State the blood parasite species.
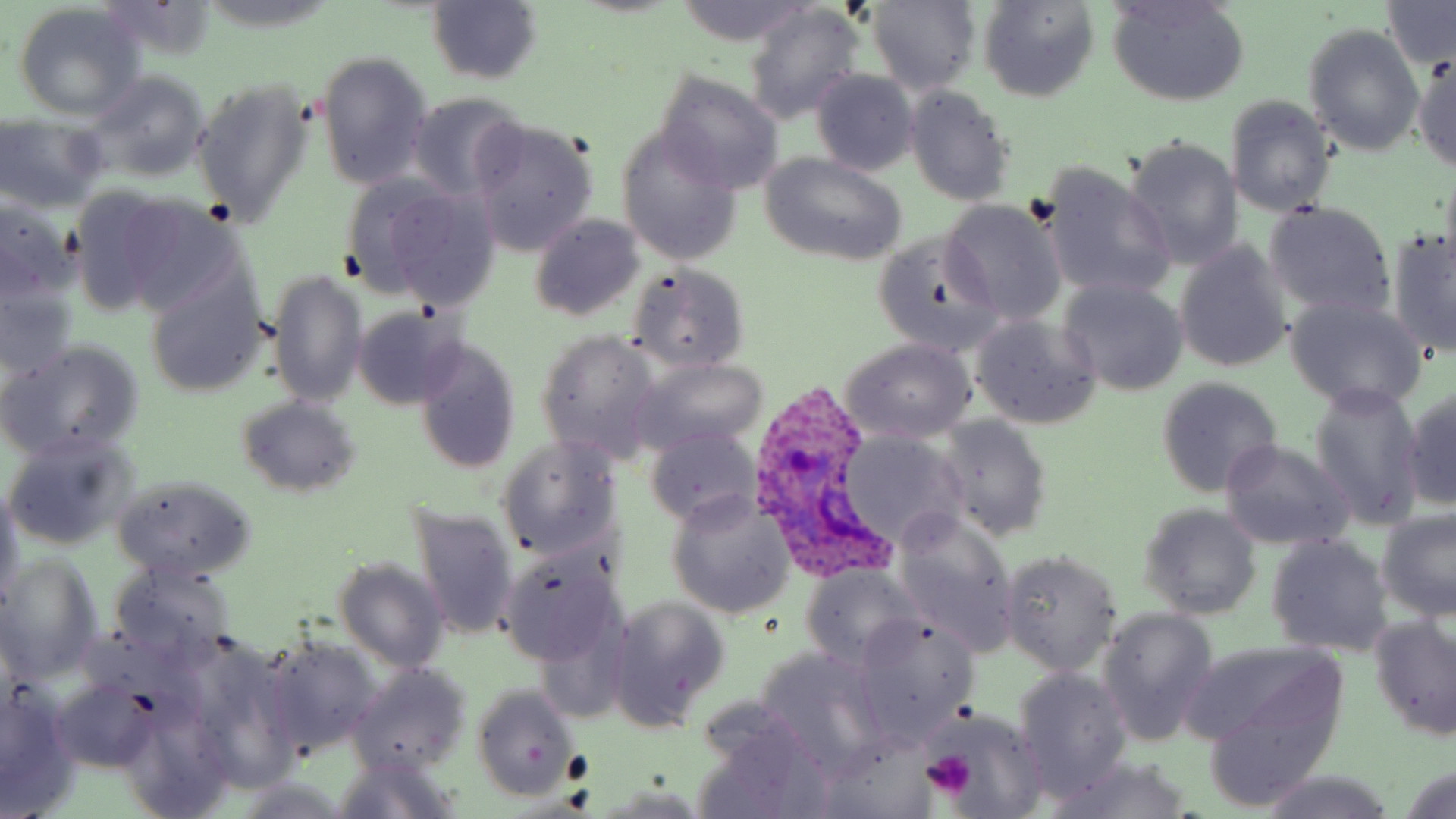
Plasmodium ovale.

Summary:
  - Coordinate format: approximate bounding boxes as named x1/y1/x2/y2 corners in pixels
  - Platelet locations: (x1=563, y1=749, x2=591, y2=787), (x1=923, y1=750, x2=977, y2=799)
  - Uninfected red blood cell locations: (x1=197, y1=0, x2=338, y2=31), (x1=676, y1=0, x2=813, y2=45), (x1=1108, y1=0, x2=1250, y2=106), (x1=94, y1=1, x2=221, y2=65), (x1=979, y1=1, x2=1099, y2=103), (x1=1381, y1=1, x2=1456, y2=70), (x1=426, y1=2, x2=543, y2=84), (x1=864, y1=2, x2=982, y2=94), (x1=742, y1=4, x2=865, y2=122), (x1=13, y1=6, x2=144, y2=120), (x1=1303, y1=24, x2=1424, y2=155), (x1=314, y1=51, x2=433, y2=190), (x1=1413, y1=53, x2=1455, y2=179), (x1=82, y1=69, x2=212, y2=183), (x1=809, y1=70, x2=921, y2=177), (x1=652, y1=71, x2=783, y2=193), (x1=192, y1=77, x2=316, y2=228), (x1=903, y1=86, x2=1015, y2=207), (x1=404, y1=91, x2=529, y2=204), (x1=1226, y1=97, x2=1335, y2=216), (x1=0, y1=119, x2=107, y2=213), (x1=470, y1=121, x2=598, y2=256), (x1=616, y1=128, x2=744, y2=265), (x1=1125, y1=136, x2=1244, y2=270), (x1=759, y1=153, x2=909, y2=267), (x1=1036, y1=160, x2=1176, y2=302), (x1=344, y1=174, x2=502, y2=310), (x1=65, y1=183, x2=185, y2=316), (x1=0, y1=195, x2=78, y2=304), (x1=113, y1=195, x2=246, y2=318), (x1=941, y1=200, x2=1066, y2=327), (x1=1263, y1=201, x2=1396, y2=321), (x1=529, y1=214, x2=647, y2=322), (x1=1386, y1=225, x2=1456, y2=360), (x1=872, y1=230, x2=1003, y2=357), (x1=1173, y1=242, x2=1292, y2=373), (x1=628, y1=264, x2=751, y2=375), (x1=269, y1=269, x2=369, y2=409), (x1=145, y1=271, x2=269, y2=398), (x1=1056, y1=280, x2=1188, y2=395), (x1=0, y1=282, x2=77, y2=381), (x1=1286, y1=297, x2=1428, y2=413), (x1=350, y1=306, x2=468, y2=409), (x1=971, y1=314, x2=1103, y2=430), (x1=536, y1=331, x2=665, y2=459), (x1=1, y1=338, x2=145, y2=463), (x1=841, y1=339, x2=976, y2=443), (x1=413, y1=340, x2=522, y2=475), (x1=632, y1=359, x2=769, y2=456), (x1=1155, y1=377, x2=1282, y2=497), (x1=1308, y1=380, x2=1428, y2=529), (x1=1404, y1=388, x2=1456, y2=514), (x1=235, y1=395, x2=362, y2=498), (x1=937, y1=417, x2=1052, y2=541), (x1=643, y1=426, x2=765, y2=529), (x1=4, y1=433, x2=137, y2=550), (x1=837, y1=434, x2=967, y2=552), (x1=497, y1=437, x2=623, y2=566), (x1=1219, y1=439, x2=1353, y2=551), (x1=113, y1=474, x2=259, y2=580), (x1=0, y1=485, x2=23, y2=607), (x1=666, y1=492, x2=797, y2=618), (x1=407, y1=502, x2=522, y2=642), (x1=1140, y1=504, x2=1261, y2=620), (x1=1377, y1=509, x2=1456, y2=620), (x1=891, y1=511, x2=1020, y2=656), (x1=1265, y1=533, x2=1395, y2=657), (x1=496, y1=545, x2=628, y2=672), (x1=1001, y1=551, x2=1122, y2=675), (x1=0, y1=555, x2=102, y2=681), (x1=332, y1=558, x2=450, y2=672), (x1=109, y1=561, x2=235, y2=666), (x1=799, y1=564, x2=928, y2=669), (x1=606, y1=596, x2=730, y2=730), (x1=1096, y1=608, x2=1219, y2=744), (x1=1369, y1=614, x2=1456, y2=739), (x1=852, y1=616, x2=981, y2=748), (x1=259, y1=632, x2=383, y2=757), (x1=753, y1=648, x2=891, y2=774), (x1=1195, y1=653, x2=1349, y2=802), (x1=345, y1=663, x2=472, y2=779), (x1=1012, y1=668, x2=1133, y2=801), (x1=53, y1=677, x2=159, y2=772), (x1=0, y1=685, x2=81, y2=816), (x1=473, y1=685, x2=579, y2=803), (x1=115, y1=696, x2=233, y2=818), (x1=929, y1=708, x2=1050, y2=814), (x1=694, y1=713, x2=838, y2=817), (x1=327, y1=757, x2=462, y2=819), (x1=1045, y1=757, x2=1197, y2=819), (x1=1402, y1=767, x2=1456, y2=819), (x1=1253, y1=773, x2=1399, y2=818), (x1=230, y1=777, x2=355, y2=817)
  - Plasmodium ovale-infected red blood cell locations: (x1=747, y1=384, x2=892, y2=578)
  - Image size: 1456×819 pixels
  - Preparation: thin blood film
  - Magnification: 1000x
  - Modality: light microscopy
  - Stain: May-Grünwald-Giemsa
  - Field of view: single